Assess this cell for malaria.
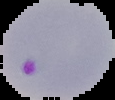

Parasitized.

{
  "preparation": "thin blood smear",
  "image_type": "segmented cell region on a black background",
  "image_size": "115×100 pixels"
}